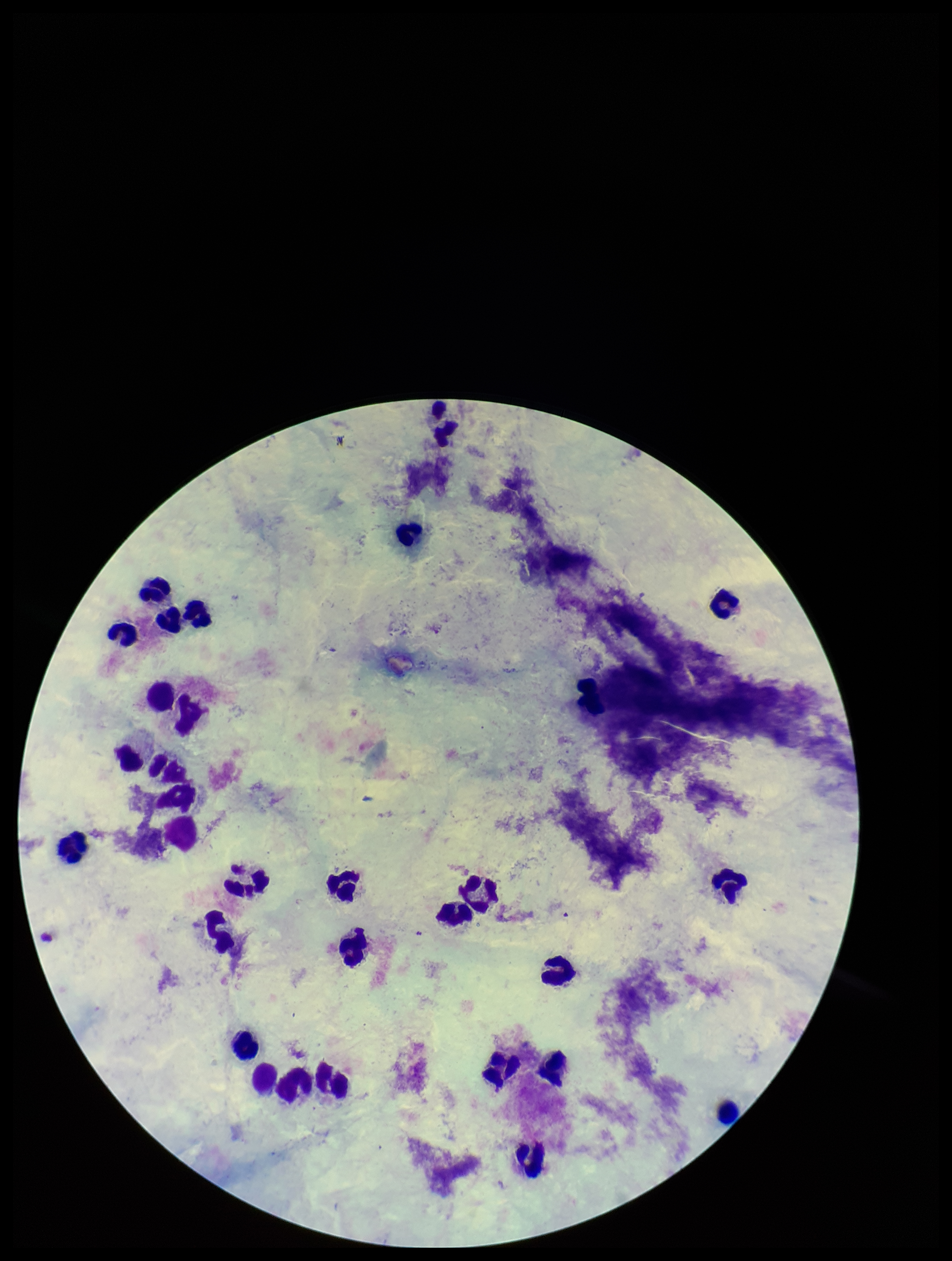
Parasite count: 0. Patient malaria status: negative. Image is 952×1261 pixels. Plasmodium parasites: none detected. Photographed through the microscope eyepiece with a smartphone camera. Leukocyte count: 29. Giemsa stain. Preparation: thick blood smear. One field from this slide.